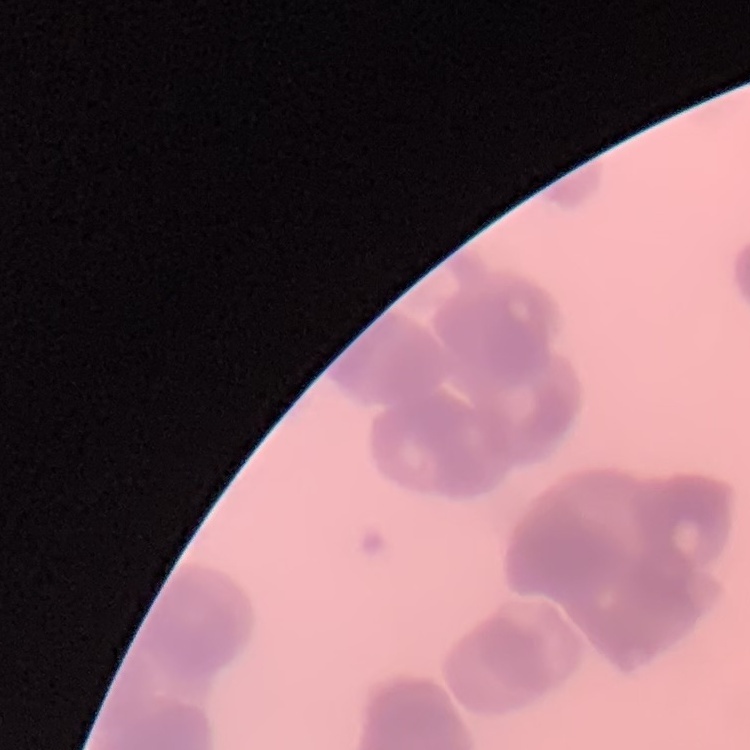 The red blood cells exhibit rouleaux formation. One tile cut from a larger photomicrograph. Stained with either Field's or Giemsa. Thin blood smear.